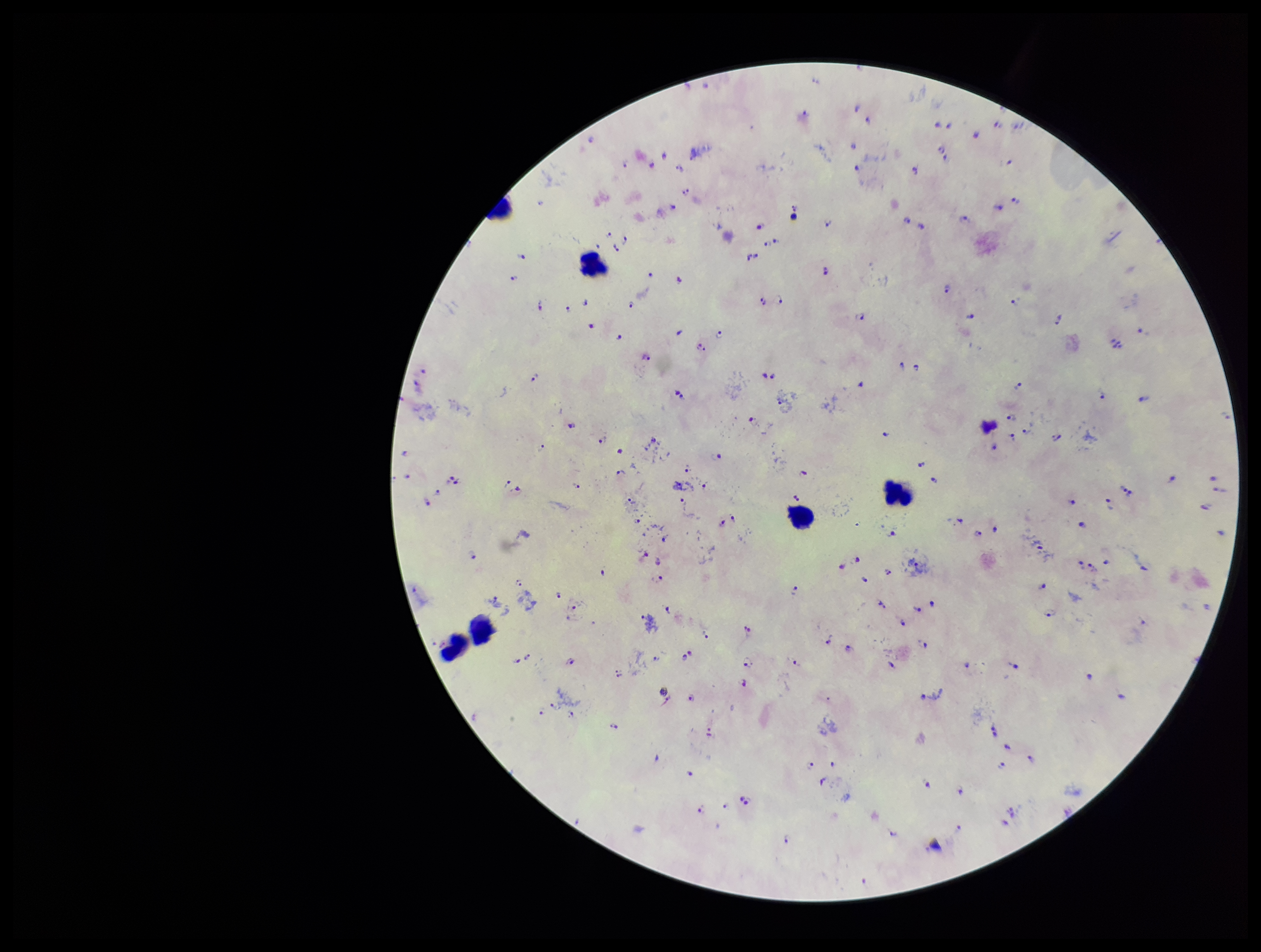
Preparation: thick blood smear. Parasite count: 126. Species reported for this patient: Plasmodium falciparum. Leukocyte count: 6. Plasmodium parasites: detected. Photographed through the microscope eyepiece with a smartphone camera. One field from this slide. Patient malaria status: positive. Stained with Giemsa. Image is 1261×952 pixels.